Classify this cell by malaria status.
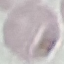
It is uninfected.

stain = Giemsa
preparation = thin smear
image type = automatically extracted cell patch, resized to 64 × 64 pixels
capture = smartphone through the microscope eyepiece